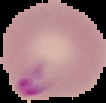 From a thin blood film. Image is 106×103 pixels. Cell region segmented out of the field of view; the surrounding area is masked to black. Result: malaria parasites detected.